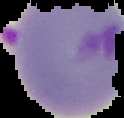
Summary:
  - Image type: segmented cell region on a black background
  - Image size: 124×118 pixels
  - Preparation: thin blood smear
  - Result: malaria parasites identified